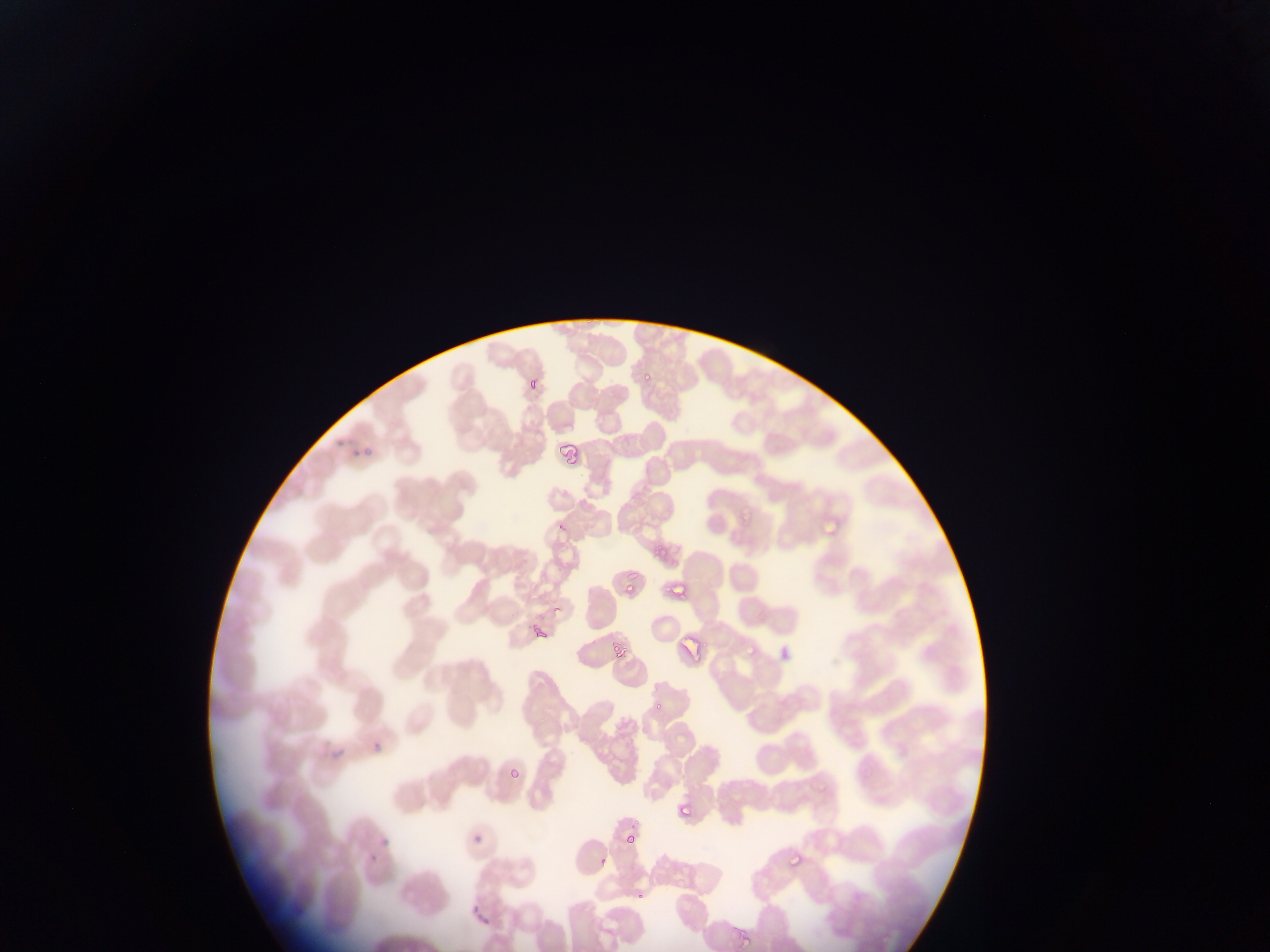
Approximate bounding boxes as [left, top, right, bottom] in pixels. Plasmodium parasite locations: [641, 367, 653, 381], [528, 381, 537, 395], [356, 450, 373, 457], [735, 510, 749, 522], [820, 511, 838, 535], [557, 520, 568, 535], [651, 543, 665, 561], [665, 584, 687, 596], [622, 585, 640, 597], [532, 616, 549, 638], [681, 633, 702, 656], [612, 639, 627, 658], [739, 639, 758, 657], [367, 739, 383, 751], [324, 747, 352, 759], [505, 760, 525, 780], [813, 779, 828, 796], [677, 802, 693, 817], [624, 832, 637, 845], [472, 835, 481, 844], [379, 838, 395, 849], [369, 850, 378, 861], [786, 852, 801, 872], [597, 856, 609, 868], [635, 894, 643, 900], [471, 905, 491, 925], [732, 927, 754, 952]. Sample from Ghana. Mobile-phone photograph taken through the microscope. One field of view. Image is 1270×952 pixels. Thin blood smear.